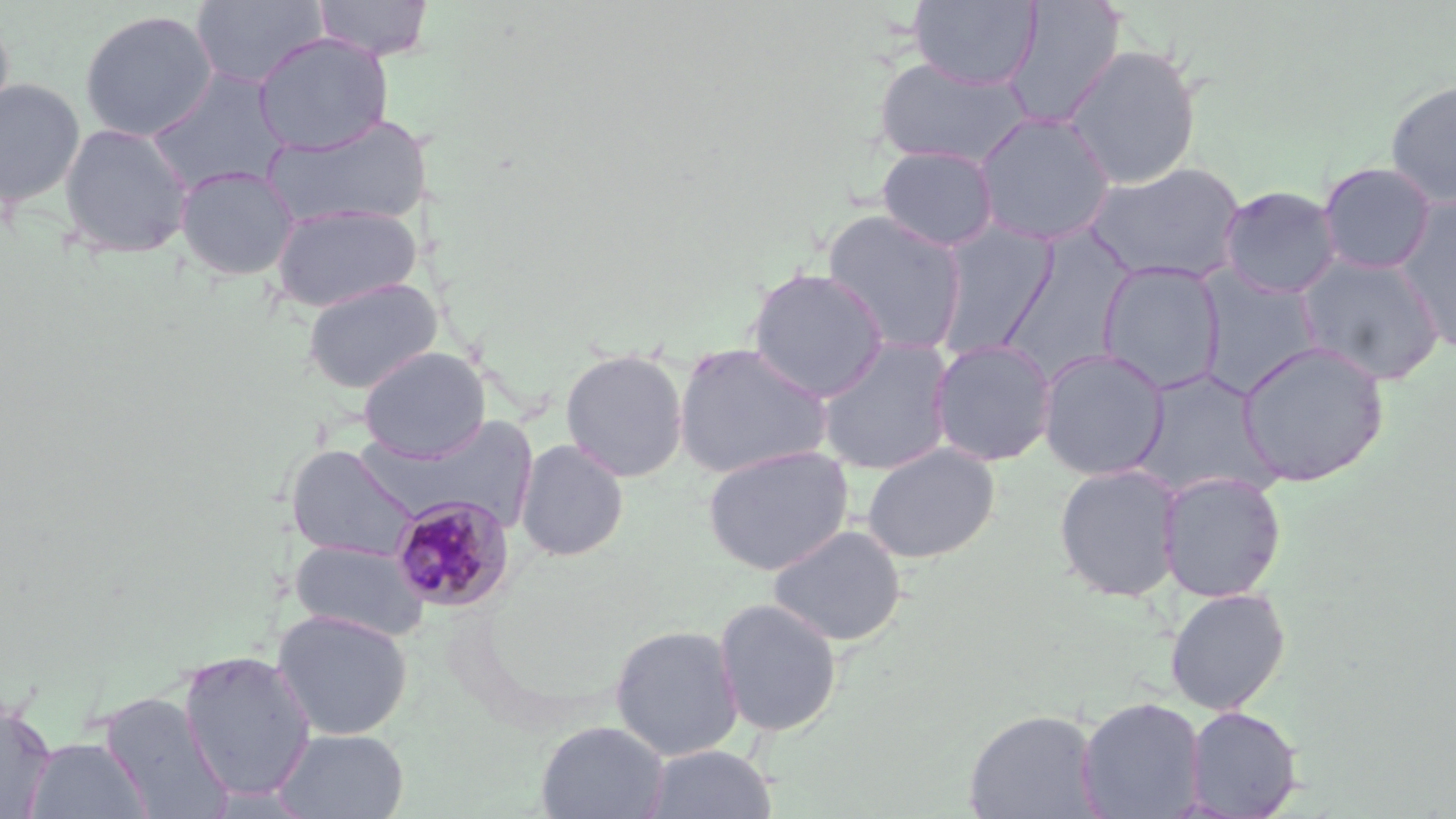
Approximate bounding boxes as (x1,y1)-(x2,y2) corner pairs in pixels. Uninfected red blood cell locations: (190,0)-(329,89), (311,0)-(436,60), (908,0)-(1043,90), (1003,0)-(1126,130), (79,9)-(218,142), (0,11)-(15,131), (253,32)-(393,155), (1063,44)-(1202,189), (872,56)-(1034,170), (146,69)-(291,195), (0,78)-(85,208), (1385,79)-(1456,208), (974,111)-(1116,246), (264,113)-(433,231), (58,122)-(194,258), (876,145)-(999,252), (1083,161)-(1247,286), (1318,161)-(1437,274), (175,165)-(299,281), (1218,185)-(1341,300), (1393,199)-(1456,355), (270,202)-(423,313), (822,210)-(968,355), (932,222)-(1057,356), (997,230)-(1135,385), (1295,255)-(1445,387), (1097,261)-(1226,394), (746,267)-(889,402), (1196,267)-(1324,397), (303,277)-(443,394), (815,337)-(955,475), (929,339)-(1057,466), (1236,341)-(1390,487), (673,342)-(834,480), (358,346)-(490,462), (560,348)-(689,482), (1038,348)-(1170,481), (1130,368)-(1279,500), (370,415)-(540,534), (515,440)-(629,561), (862,442)-(1000,564), (286,444)-(420,562), (702,445)-(854,576), (1053,463)-(1184,602), (1158,471)-(1286,603), (767,524)-(906,648), (290,538)-(428,642), (1164,587)-(1291,715), (713,598)-(843,737), (273,609)-(412,741), (609,624)-(744,761), (178,649)-(316,802), (99,691)-(233,818), (1076,696)-(1206,818), (0,699)-(57,817), (1184,705)-(1302,817), (964,708)-(1103,818), (535,720)-(669,819), (272,728)-(410,819), (24,735)-(151,819), (641,744)-(778,819). Plasmodium malariae-infected red blood cell locations: (388,495)-(515,614). Slide-level diagnosis: Plasmodium malariae. May-Grünwald-Giemsa stain. One field of a larger specimen. Image is 1456×819 pixels. Thin blood smear. Captured at 1000x magnification. Optical microscopy.